Report the malaria status of this cell.
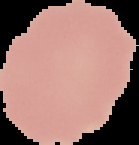

It is uninfected.

preparation = thin blood film
image size = 139×145 pixels
image type = segmented cell region with the area outside set to black